Locate every blood parasite and identify its species.
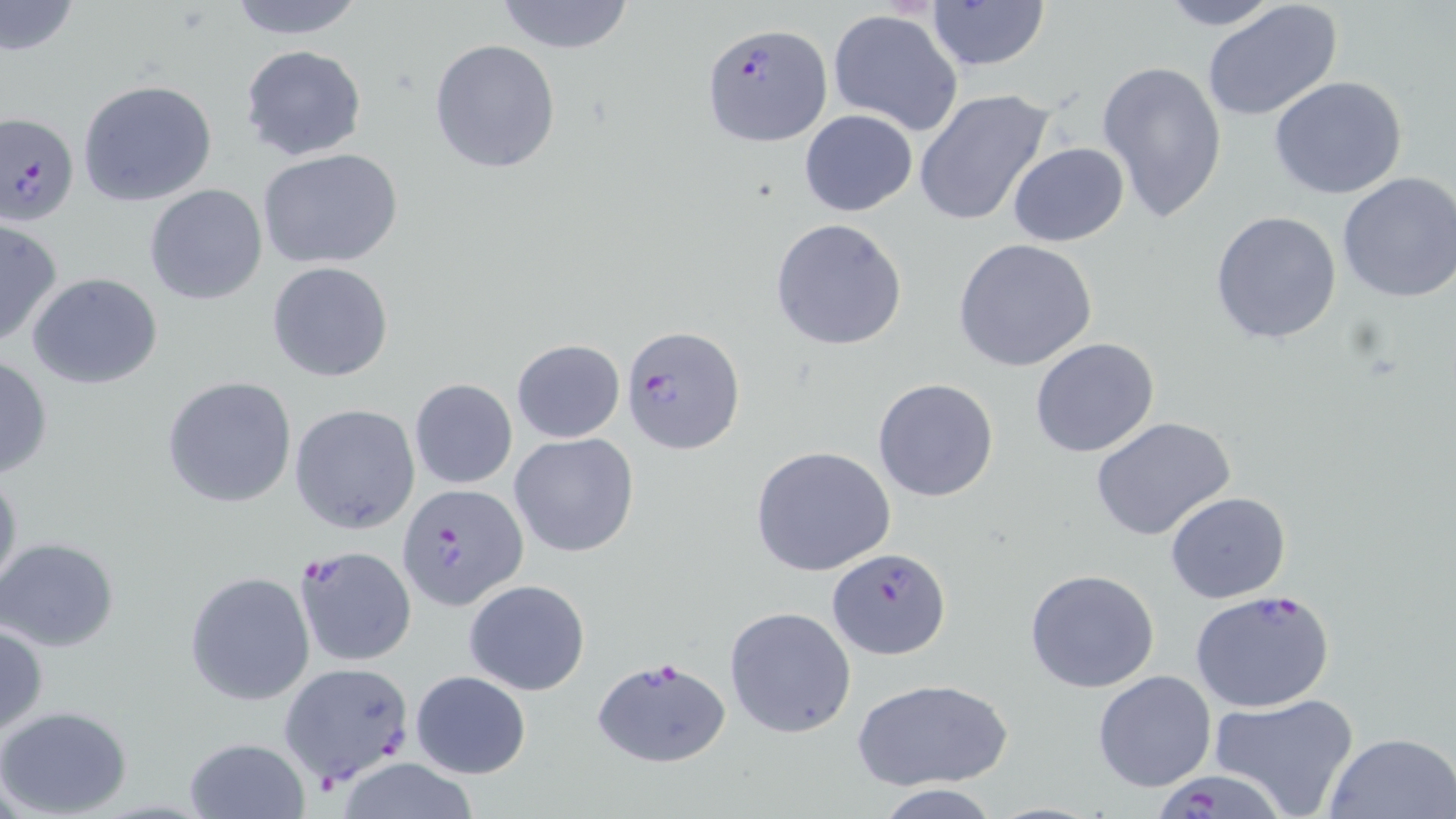
Approximate bounding boxes as (x1, y1, x2, y2) in pixels.
Plasmodium falciparum-infected red blood cells: (703, 23, 832, 148), (0, 112, 80, 225), (620, 323, 745, 455), (398, 483, 528, 611), (294, 544, 416, 668), (826, 547, 950, 659), (1189, 589, 1337, 714), (591, 655, 731, 770), (281, 662, 416, 784), (1150, 763, 1287, 819).
No Plasmodium ovale, Plasmodium malariae, Plasmodium vivax, Babesia divergens, or Trypanosoma brucei observed.

Summary:
  - Uninfected red blood cell locations: (221, 0, 369, 40), (493, 0, 638, 54), (924, 0, 1051, 74), (1152, 0, 1289, 30), (0, 1, 81, 60), (1202, 1, 1343, 123), (828, 8, 965, 137), (430, 38, 562, 175), (239, 44, 367, 163), (1097, 61, 1228, 226), (1268, 76, 1409, 200), (77, 78, 217, 206), (913, 89, 1056, 227), (799, 109, 918, 217), (1008, 141, 1129, 246), (256, 148, 404, 270), (1335, 171, 1456, 304), (145, 185, 269, 304), (1211, 209, 1343, 345), (0, 215, 63, 349), (770, 218, 908, 351), (954, 239, 1099, 372), (268, 262, 393, 382), (27, 273, 164, 389), (1030, 337, 1161, 458), (512, 339, 625, 443), (0, 354, 52, 481), (161, 376, 299, 508), (409, 378, 517, 490), (873, 379, 999, 503), (290, 404, 421, 533), (1091, 417, 1238, 542), (509, 432, 640, 558), (750, 445, 898, 579), (0, 464, 22, 603), (1165, 490, 1290, 603), (0, 537, 120, 652), (1024, 568, 1162, 695), (185, 571, 315, 705), (464, 579, 590, 696), (724, 606, 858, 738), (0, 622, 48, 737), (1093, 669, 1216, 791), (411, 670, 531, 780), (855, 677, 1012, 789), (1207, 692, 1361, 819), (0, 705, 133, 817), (1323, 731, 1456, 818), (185, 735, 310, 818), (331, 758, 484, 819), (869, 783, 1004, 818)
  - Slide-level diagnosis: Plasmodium falciparum
  - Preparation: thin blood smear
  - Stain: May-Grünwald-Giemsa
  - Field of view: single
  - Image size: 1456×819 pixels
  - Modality: optical microscopy
  - Magnification: 1000x